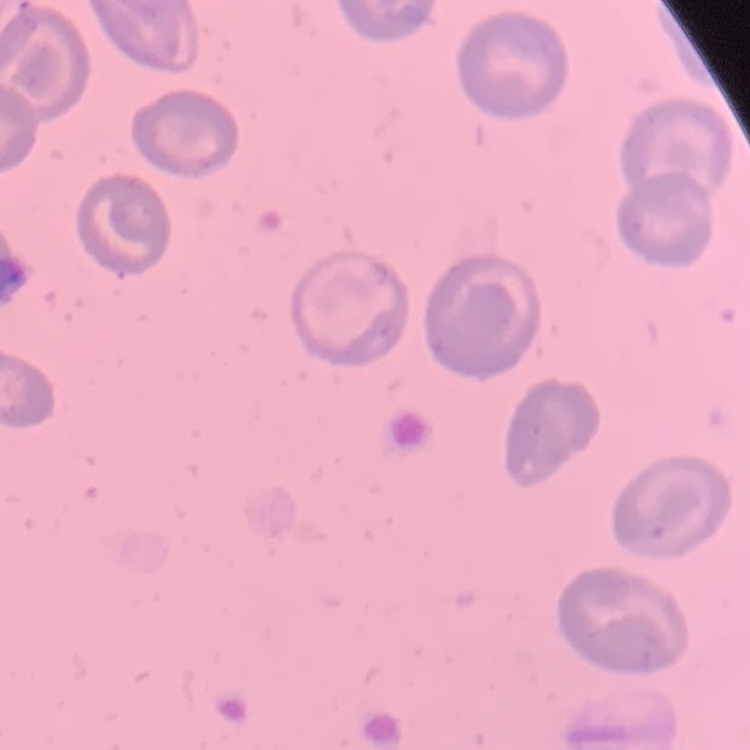
Summary:
  - Erythrocyte morphology: no rouleaux formation
  - Preparation: thin blood smear
  - Image type: square crop of a larger photomicrograph
  - Stain: Field's or Giemsa